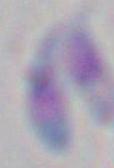
magnification: 1000x
modality: micrograph
identification: Toxoplasma gondii